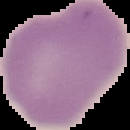 From a thin blood smear. Segmented cell region on a black background. Malaria status: uninfected. Image is 130×130 pixels.